Describe the morphology of the red blood cells.
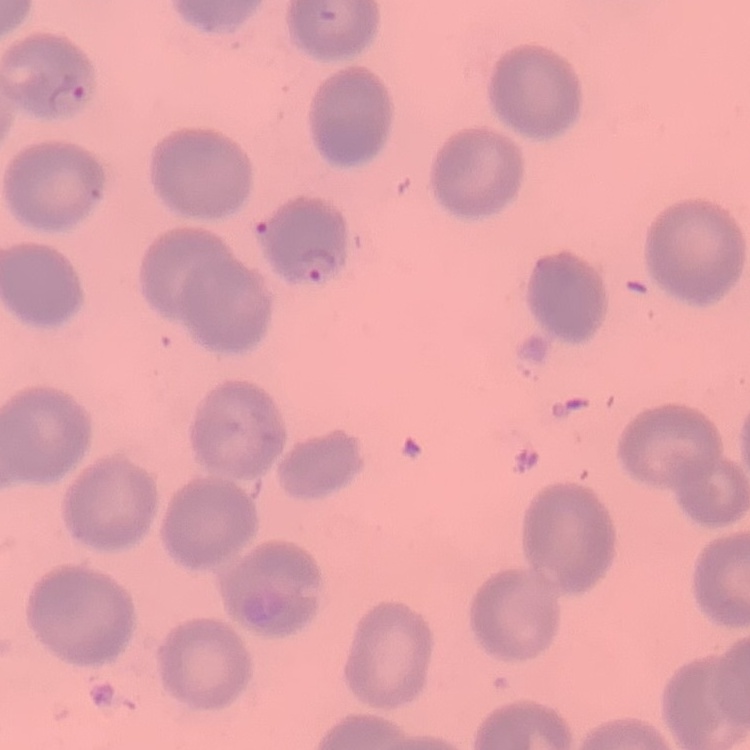

No rouleaux formation.

{
  "stain": "Field's or Giemsa",
  "preparation": "thin blood smear",
  "image_type": "square crop of a larger photomicrograph"
}